State the preparation type.
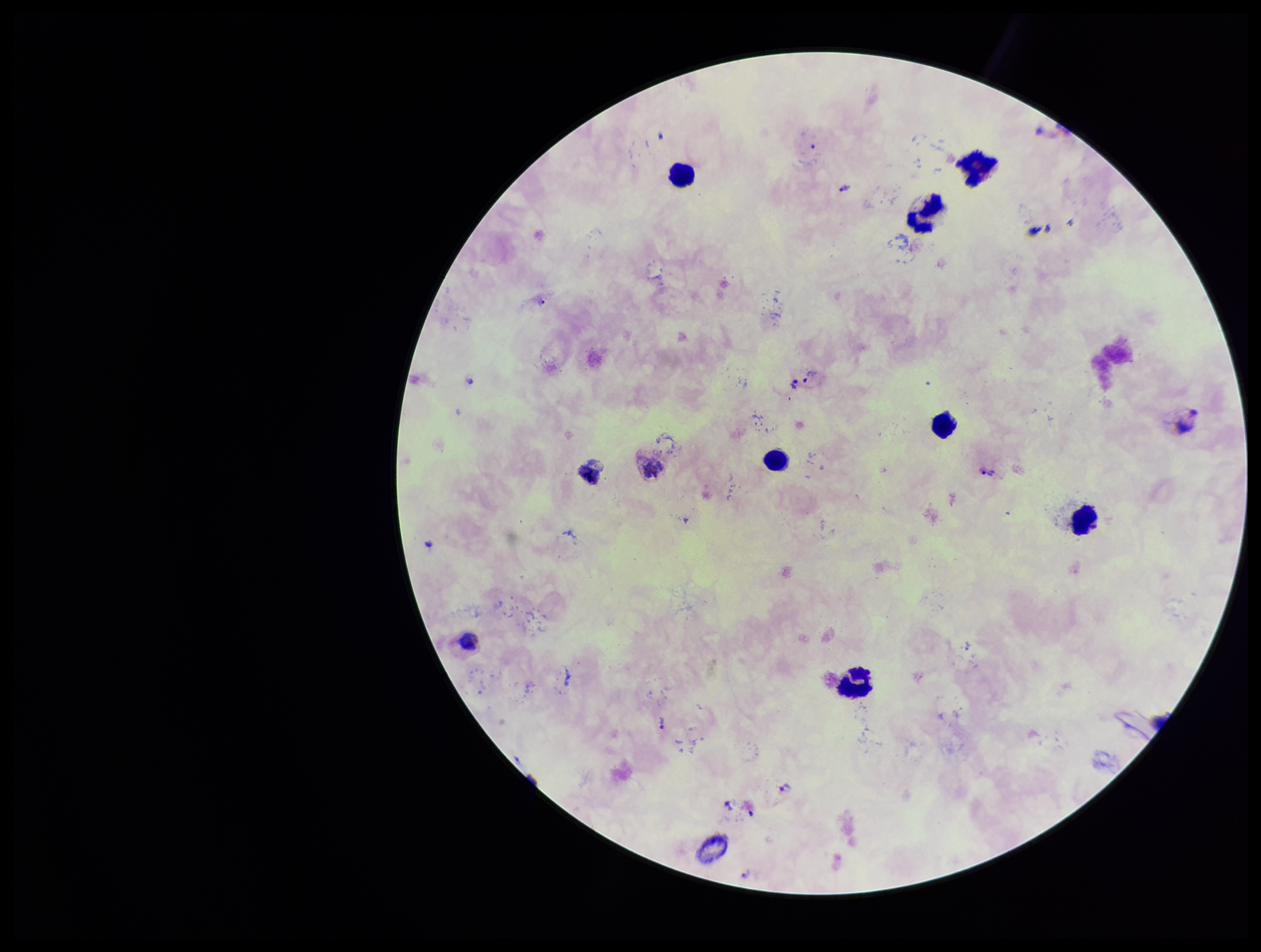

A thick smear.

Patient malaria status: infected. Photographed through the microscope eyepiece with a smartphone camera. Species reported for this patient: Plasmodium vivax. Stained with Giemsa. Plasmodium parasites: identified. Leukocyte count: 10. Image is 1261×952 pixels. Parasite count: 9. One field from this slide.